Assess the morphology of the erythrocytes.
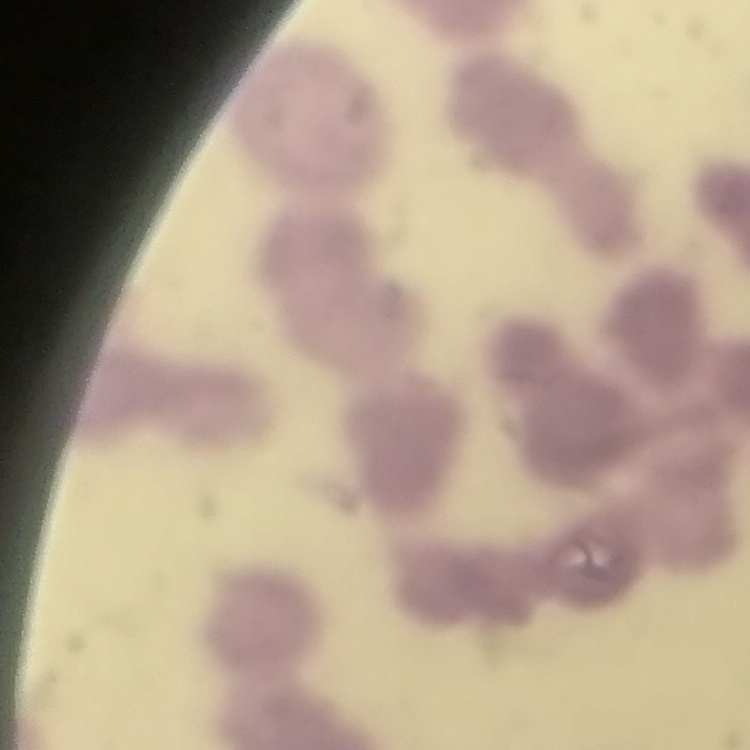
They show rouleaux formation.

One tile cut from a larger photomicrograph. Thin blood smear. Stained with either Field's or Giemsa.